Give the extent of all uninfected red blood cells.
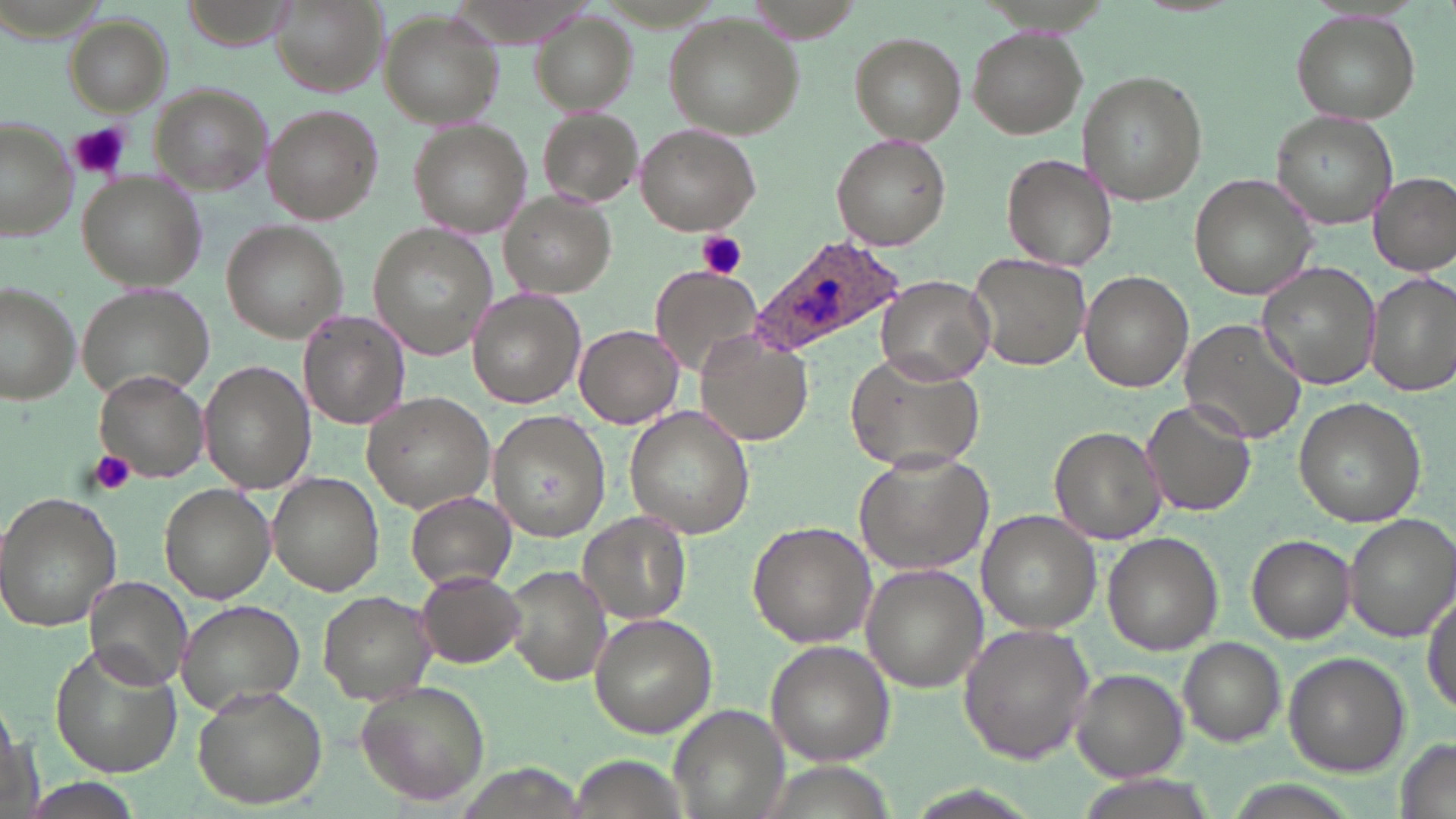
Approximate bounding boxes as (x1, y1, x2, y2) in pixels.
Uninfected red blood cells: (269, 1, 384, 97), (530, 10, 638, 112), (1290, 10, 1422, 125), (379, 11, 504, 128), (663, 12, 805, 139), (65, 14, 173, 117), (967, 26, 1086, 138), (850, 34, 965, 142), (1077, 72, 1205, 206), (147, 84, 268, 195), (262, 104, 383, 223), (536, 107, 643, 210), (1272, 111, 1394, 229), (1, 115, 79, 244), (408, 123, 532, 239), (635, 124, 761, 236), (830, 133, 951, 251), (1002, 153, 1117, 271), (78, 170, 206, 289), (1187, 172, 1318, 302), (1368, 172, 1456, 275), (503, 192, 615, 299), (220, 221, 344, 343), (366, 225, 495, 361), (968, 251, 1091, 372), (1255, 262, 1382, 390), (650, 265, 761, 376), (1079, 271, 1194, 392), (1365, 271, 1456, 396), (876, 276, 995, 381), (0, 284, 81, 404), (77, 285, 215, 404), (468, 290, 585, 406), (298, 308, 410, 429), (1181, 317, 1308, 445), (573, 325, 683, 428), (695, 337, 810, 445), (846, 350, 985, 474), (199, 360, 316, 493), (96, 373, 210, 479), (363, 392, 498, 513), (1292, 396, 1426, 527), (1140, 397, 1257, 518), (623, 405, 753, 538), (489, 410, 611, 540), (1048, 425, 1168, 544), (854, 451, 992, 575), (268, 472, 384, 594), (159, 483, 277, 602), (0, 491, 124, 629), (406, 492, 514, 591), (579, 511, 692, 624), (979, 511, 1100, 633), (1345, 513, 1456, 644), (748, 521, 876, 645), (1103, 533, 1223, 654), (1246, 536, 1355, 643), (861, 562, 988, 692), (507, 566, 611, 688), (414, 568, 524, 669), (84, 575, 192, 688), (1423, 580, 1455, 720), (319, 591, 433, 700), (176, 598, 305, 716), (589, 614, 717, 737), (958, 621, 1098, 765), (1178, 636, 1286, 746), (764, 640, 895, 767), (50, 642, 184, 775), (1283, 651, 1410, 775), (1070, 667, 1187, 782), (356, 680, 492, 807), (192, 685, 328, 809), (666, 704, 790, 819), (1391, 735, 1455, 819).

Plasmodium ovale-infected red blood cell locations = approximate bounding boxes as (x1, y1, x2, y2) in pixels: (749, 233, 909, 360)
slide-level diagnosis = Plasmodium ovale
preparation = thin blood smear
platelet locations = approximate bounding boxes as (x1, y1, x2, y2) in pixels: (70, 121, 131, 179), (697, 229, 747, 281), (87, 448, 139, 497)
stain = May-Grünwald-Giemsa
modality = light microscopy
magnification = 1000x
field of view = one of a larger specimen
image size = 1456×819 pixels